Comment on the morphology of the red blood cells.
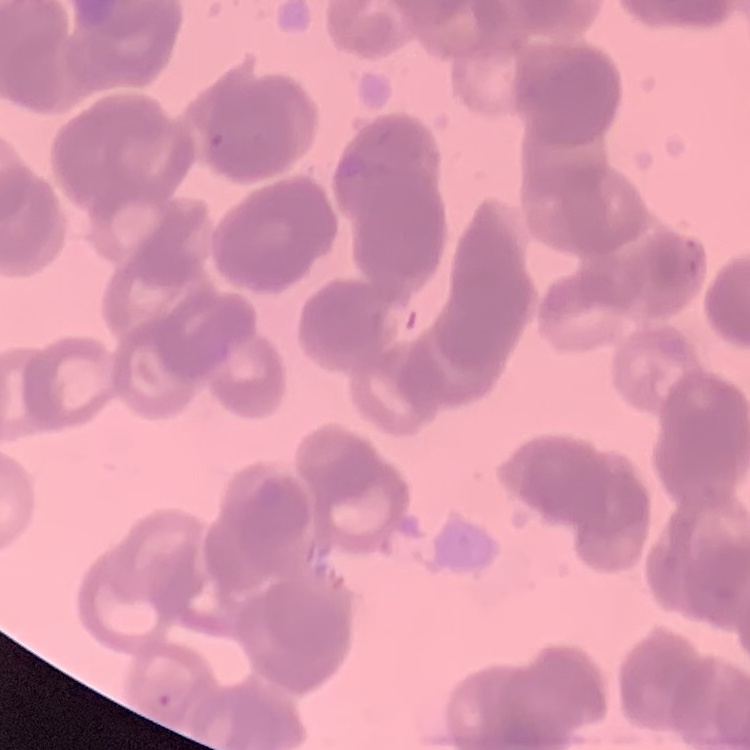

Rouleaux formation.

stain: Field's or Giemsa
preparation: thin blood film
image_type: square crop of a larger photomicrograph